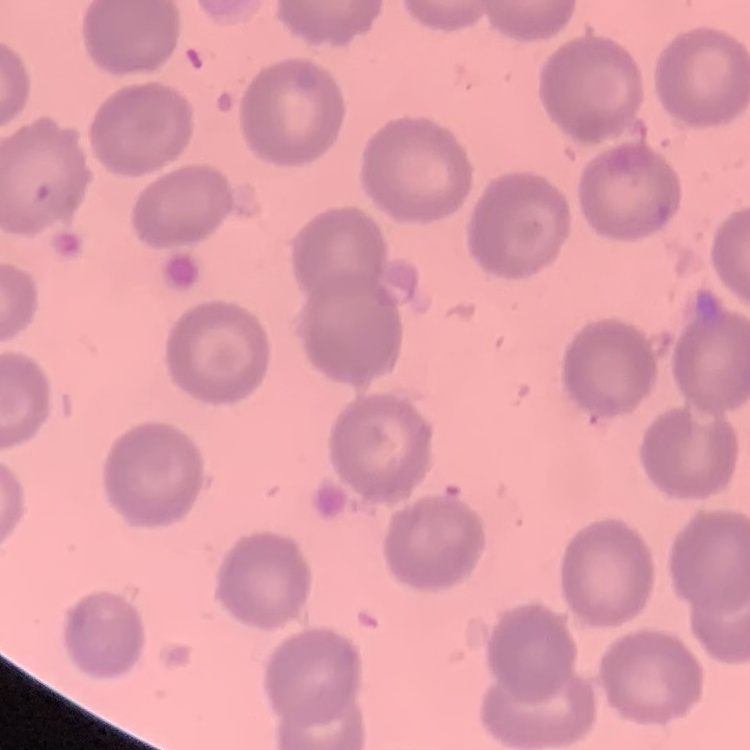

Summary:
  - Red blood cell morphology: no rouleaux formation
  - Preparation: thin peripheral smear
  - Image type: one tile cut from a larger photomicrograph
  - Stain: Field's or Giemsa